Name the parasite shown.
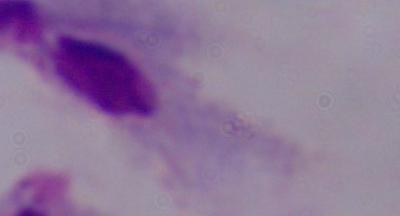

This is a trichomonad.

Photomicrograph. 1000x magnification.